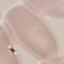

Summary:
  - Result: negative for malaria parasites
  - Preparation: thin blood film
  - Stain: Giemsa
  - Capture: smartphone camera at the microscope eyepiece
  - Image type: automatically extracted cell patch, resized to 64 × 64 pixels